Identify the blood parasite species.
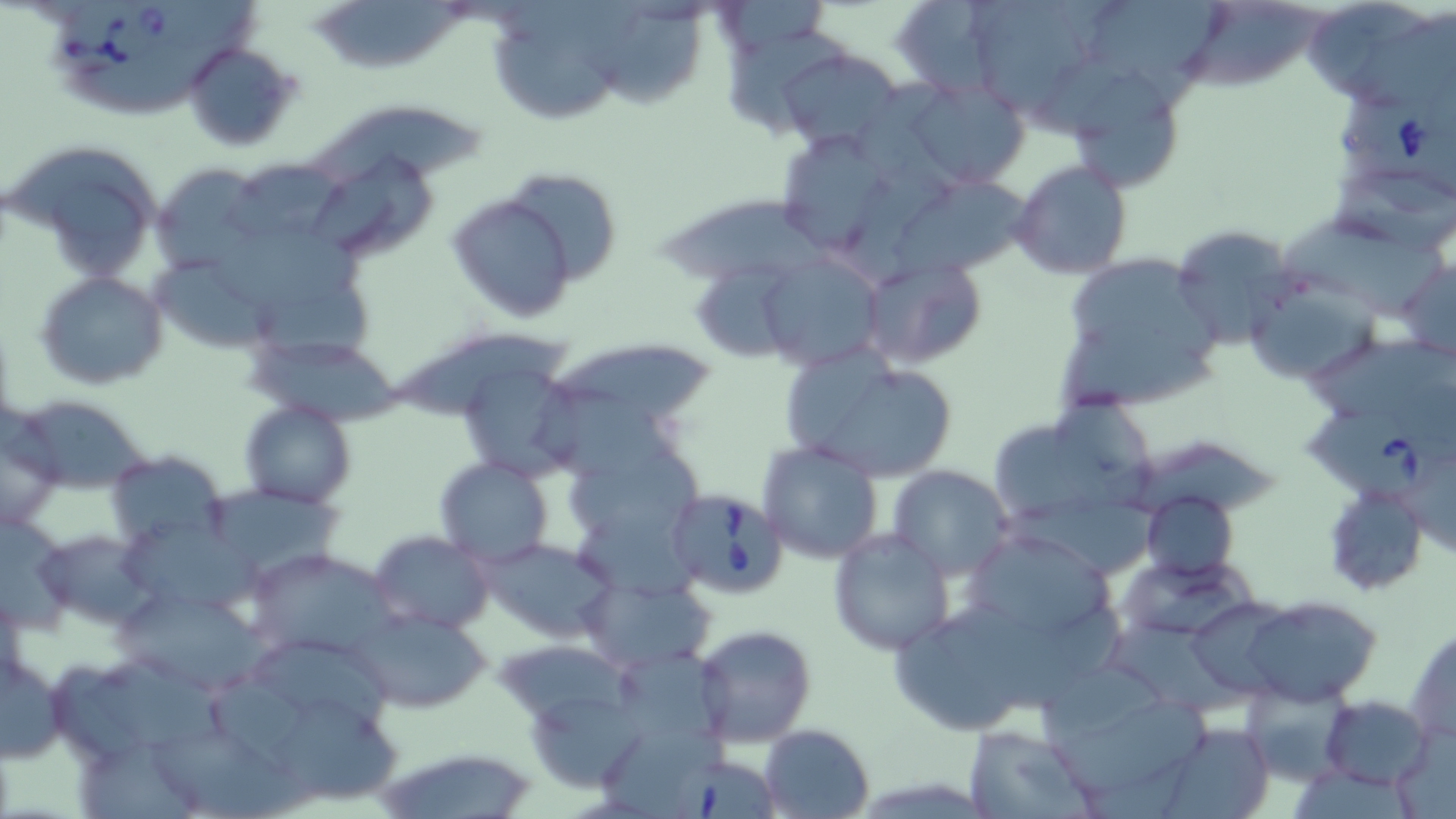

Babesia divergens.

Summary:
  - Coordinate format: approximate bounding boxes as (x1, y1, x2, y2) in pixels
  - Uninfected red blood cell locations: (888, 0, 1015, 99), (955, 0, 1103, 118), (1077, 0, 1242, 90), (1306, 0, 1450, 113), (1184, 3, 1328, 95), (311, 17, 470, 78), (596, 17, 716, 115), (725, 23, 854, 152), (492, 28, 624, 127), (181, 41, 302, 152), (776, 46, 905, 152), (1058, 62, 1190, 194), (900, 76, 1031, 190), (310, 102, 499, 200), (770, 127, 905, 261), (7, 138, 165, 281), (305, 146, 443, 266), (228, 155, 352, 250), (1010, 159, 1132, 279), (151, 162, 264, 275), (499, 168, 624, 288), (893, 170, 1034, 278), (446, 191, 579, 324), (657, 200, 858, 290), (1284, 216, 1451, 326), (1169, 224, 1298, 350), (1053, 252, 1228, 413), (760, 253, 885, 371), (1399, 253, 1456, 365), (858, 255, 988, 370), (695, 258, 804, 367), (152, 259, 288, 354), (256, 265, 383, 381), (34, 271, 169, 391), (1245, 276, 1381, 384), (393, 333, 585, 421), (544, 338, 718, 438), (247, 345, 411, 428), (780, 347, 961, 484), (449, 349, 586, 484), (1048, 388, 1170, 521), (16, 396, 154, 494), (241, 401, 354, 508), (0, 407, 65, 529), (994, 428, 1118, 529), (756, 440, 885, 565), (564, 441, 705, 557), (105, 450, 229, 549), (435, 457, 555, 566), (888, 466, 1014, 579), (202, 482, 343, 582), (1321, 482, 1429, 596), (1138, 492, 1237, 580), (953, 526, 1123, 659), (828, 527, 955, 655), (37, 528, 156, 627), (369, 530, 493, 635), (479, 537, 614, 642), (249, 547, 396, 663), (1115, 554, 1260, 643), (578, 574, 714, 674), (108, 589, 288, 692), (1241, 596, 1383, 708), (892, 604, 1043, 737), (350, 605, 488, 712), (1108, 623, 1262, 720), (694, 624, 818, 747), (1405, 626, 1456, 746), (250, 637, 406, 736), (611, 649, 734, 755), (0, 655, 67, 763), (1037, 676, 1214, 811), (1237, 682, 1354, 787), (521, 683, 653, 795), (1320, 695, 1434, 789), (270, 700, 406, 809), (151, 706, 337, 819), (1157, 721, 1275, 819), (758, 724, 874, 817), (962, 726, 1102, 818), (1387, 727, 1456, 819), (78, 736, 194, 819), (374, 743, 542, 819)
  - Babesia divergens-infected red blood cell locations: (48, 6, 186, 85), (1341, 88, 1455, 213), (1304, 405, 1456, 504), (665, 487, 791, 598), (668, 759, 779, 819)
  - Preparation: thin blood smear
  - Magnification: 1000x
  - Image size: 1456×819 pixels
  - Modality: optical microscopy
  - Stain: May-Grünwald-Giemsa
  - Field of view: single